Describe the morphology of the red blood cells.
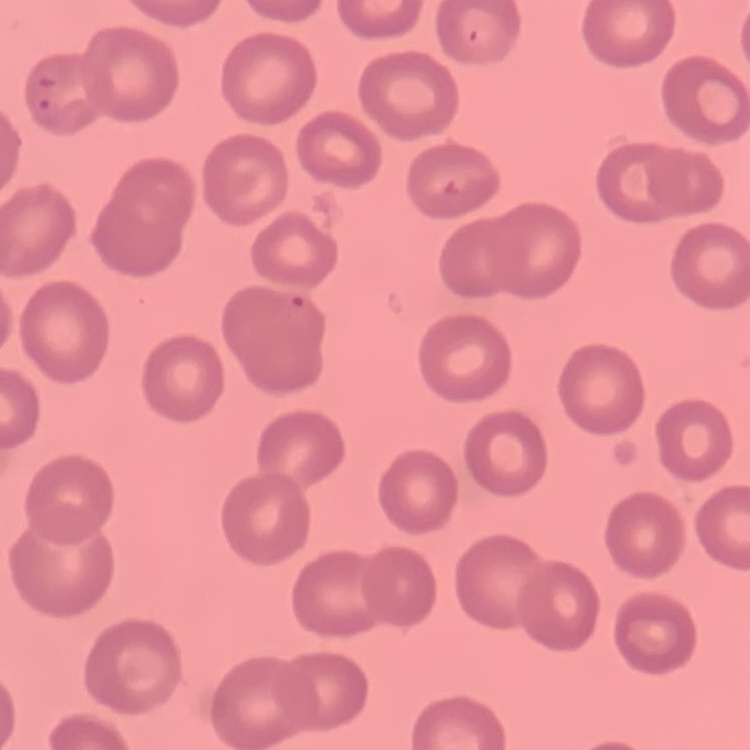
They show no rouleaux formation.

One tile cut from a larger photomicrograph. Field's or Giemsa stain. Thin peripheral smear.